Assess this cell for malaria.
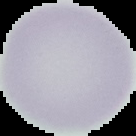

Uninfected.

image type = segmented cell region with the area outside set to black
preparation = thin blood film
image size = 136×136 pixels